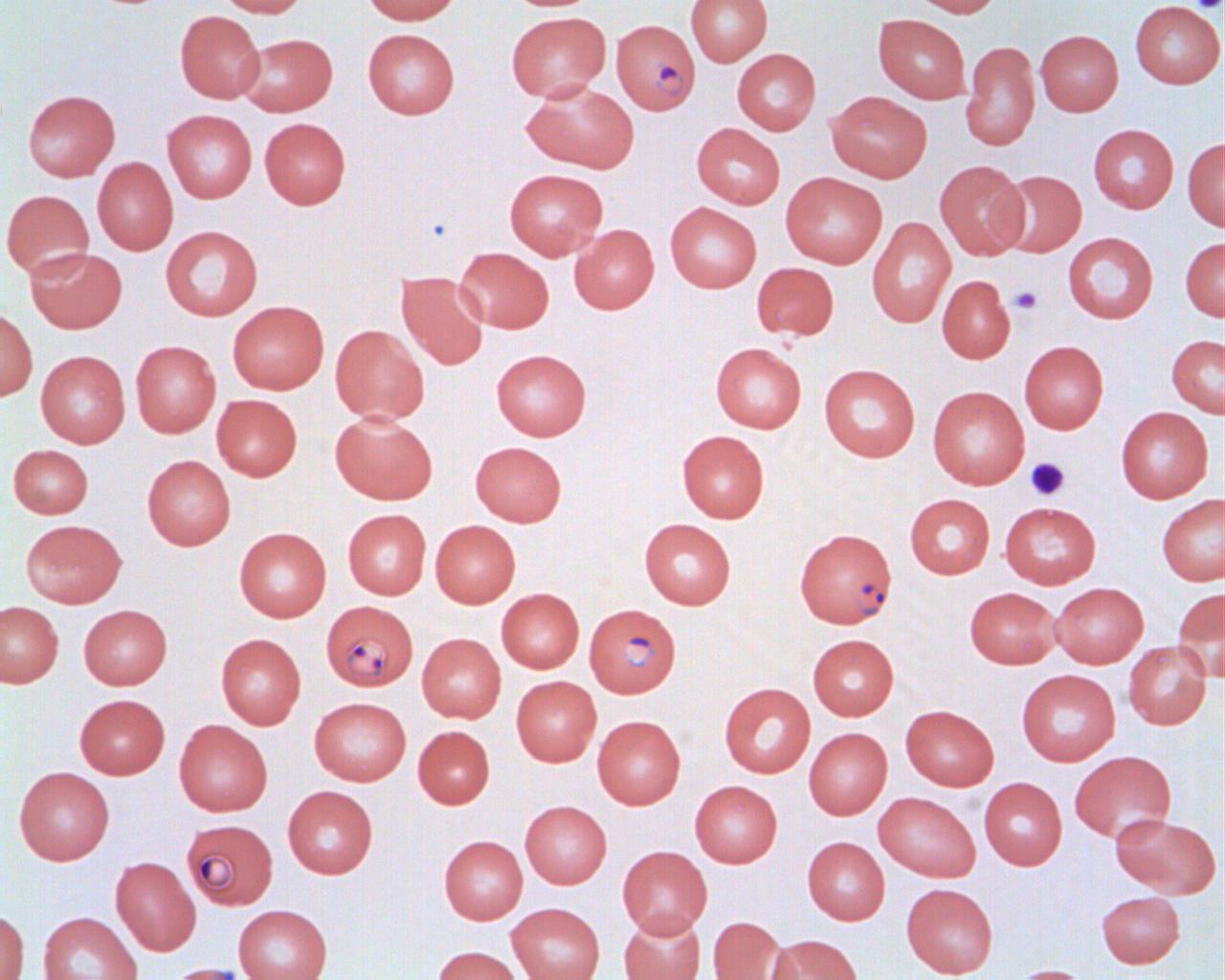

Summary:
  - Coordinate format: approximate bounding boxes as (x1,y1)-(x2,y2) corner pairs in pixels
  - Uninfected red blood cell locations: (212,0)-(307,18), (361,0)-(461,26), (686,0)-(773,66), (907,0)-(1002,18), (1130,1)-(1224,88), (175,10)-(265,103), (506,12)-(610,102), (873,14)-(971,103), (363,28)-(459,119), (1034,29)-(1123,116), (237,33)-(338,116), (960,40)-(1040,151), (732,48)-(821,134), (521,82)-(639,173), (22,89)-(120,181), (826,91)-(932,183), (162,109)-(258,203), (259,117)-(351,209), (691,123)-(785,209), (1088,124)-(1178,213), (1183,136)-(1225,231), (92,157)-(178,255), (935,160)-(1029,259), (503,168)-(608,260), (996,170)-(1087,256), (780,172)-(887,268), (1,189)-(94,280), (665,202)-(762,293), (867,216)-(955,328), (569,224)-(659,314), (160,225)-(263,321), (1063,232)-(1157,324), (1180,237)-(1225,321), (454,246)-(554,333), (25,247)-(127,333), (751,262)-(839,341), (397,272)-(489,370), (937,275)-(1015,363), (227,301)-(329,394), (0,307)-(38,401), (330,324)-(429,425), (1166,334)-(1225,418), (130,340)-(221,438), (1019,340)-(1109,434), (710,342)-(806,433), (491,349)-(591,441), (36,350)-(130,448), (819,364)-(920,462), (927,386)-(1030,489), (212,394)-(302,481), (1115,407)-(1213,503), (330,411)-(437,505), (677,430)-(769,523), (470,441)-(566,526), (8,444)-(93,518), (142,455)-(235,550), (905,493)-(995,578), (1157,493)-(1225,585), (1000,502)-(1100,589), (342,509)-(431,599), (640,518)-(736,609), (20,519)-(126,608), (430,519)-(520,607), (234,527)-(331,622), (1050,582)-(1148,668), (964,587)-(1061,669), (1172,587)-(1224,680), (496,588)-(584,673), (0,601)-(63,688), (78,604)-(172,690), (215,633)-(306,729), (417,633)-(506,723), (807,633)-(898,720), (1124,641)-(1211,729), (1016,669)-(1120,766), (511,676)-(601,766), (719,682)-(816,778), (74,694)-(169,779), (309,697)-(411,786), (901,705)-(999,791), (592,715)-(685,809), (174,719)-(273,816), (413,726)-(495,809), (804,727)-(892,819), (1069,750)-(1176,843), (13,766)-(114,865), (979,777)-(1066,870), (690,780)-(782,867), (283,785)-(378,879), (874,792)-(981,881), (520,800)-(611,888), (1110,813)-(1219,898), (439,835)-(528,924), (802,836)-(890,925), (617,845)-(712,938), (110,856)-(201,956), (901,883)-(998,978), (1096,891)-(1185,968), (506,903)-(605,980), (233,905)-(332,980), (0,909)-(30,980), (37,912)-(142,980), (618,912)-(706,980), (708,916)-(789,980), (766,934)-(862,980), (432,945)-(523,980), (164,963)-(257,980), (1009,964)-(1093,980)
  - Platelet locations: (1190,0)-(1224,13), (1009,286)-(1042,315), (1025,457)-(1071,501)
  - Plasmodium falciparum-infected red blood cell locations: (611,19)-(700,114), (794,528)-(897,628), (323,599)-(424,694), (584,603)-(681,697), (186,817)-(283,908)
  - Slide-level diagnosis: Plasmodium falciparum
  - Image size: 1225×980 pixels
  - Field of view: single
  - Modality: optical microscopy
  - Magnification: 1000x
  - Preparation: thin blood smear